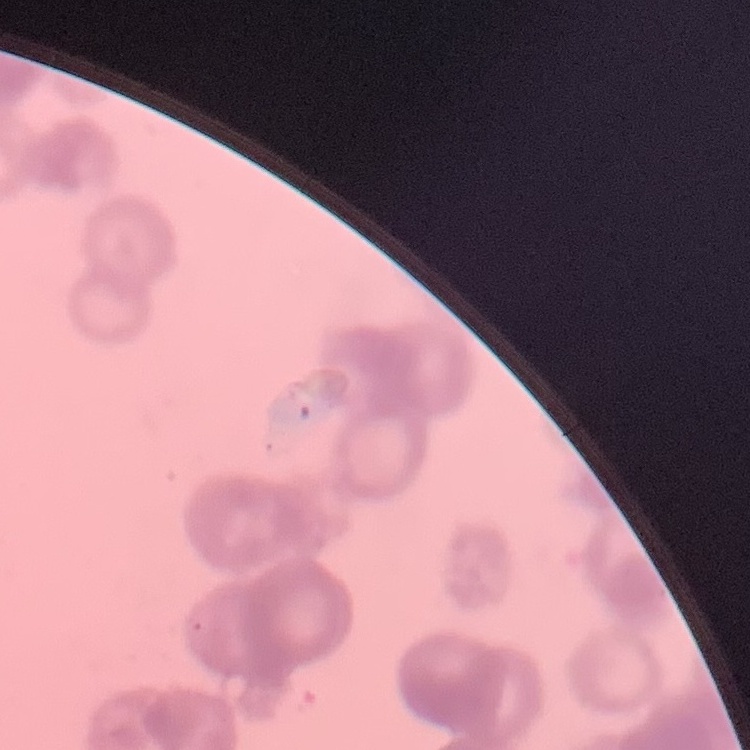

Summary:
  - Red blood cell morphology: rouleaux formation
  - Preparation: thin peripheral smear
  - Image type: square crop of a larger photomicrograph
  - Stain: Field's or Giemsa